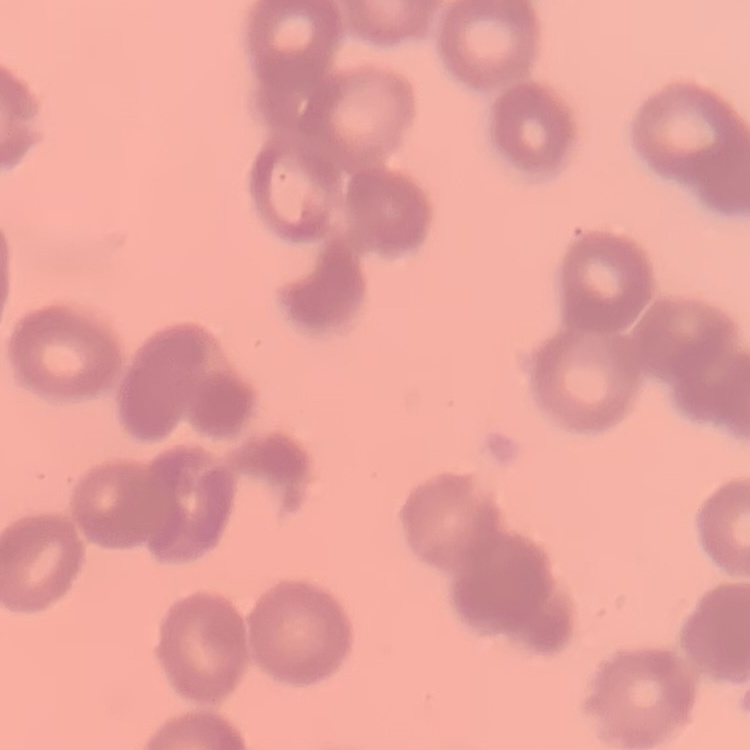 The red blood cells show rouleaux formation. Field's or Giemsa stain. Thin peripheral smear. Square crop of a larger photomicrograph.